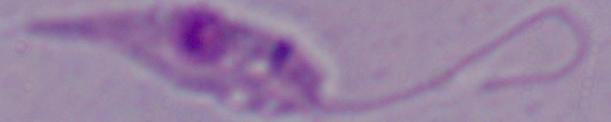
A Leishmania parasite is shown. Photomicrograph. Captured at 1000x magnification.